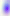

Summary:
  - Modality: micrograph
  - Magnification: 400x
  - Identification: Toxoplasma gondii